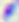
{
  "identification": "Toxoplasma gondii",
  "modality": "photomicrograph",
  "magnification": "400x"
}